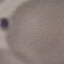

result = no malaria parasites detected
preparation = thin blood smear
stain = Giemsa
image type = cell patch, automatically extracted from a larger field of view and resized to 64 × 64 pixels
capture = smartphone camera at the microscope eyepiece